Locate every leukocyte (white blood cell).
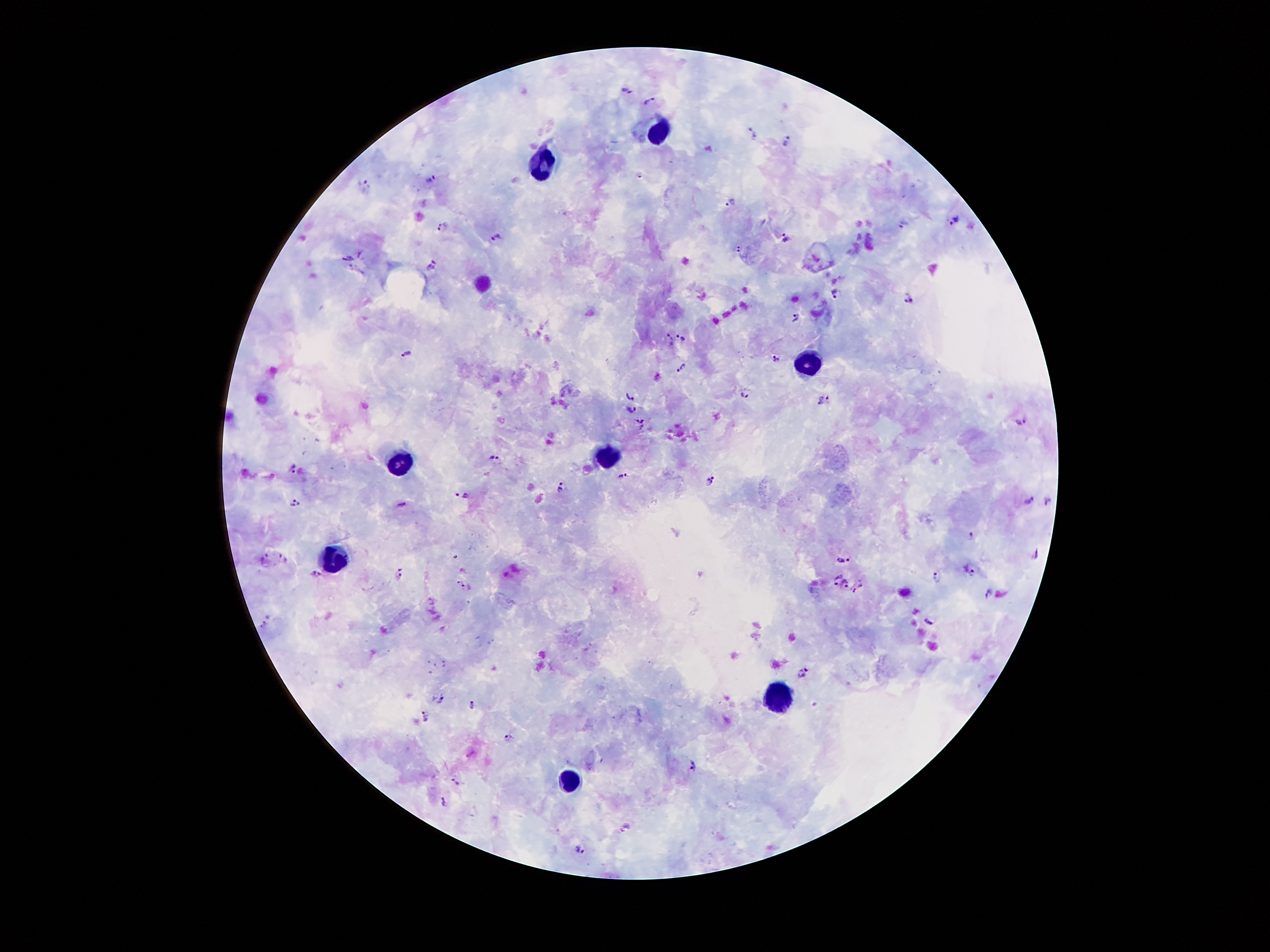

Approximate centers as (x, y) in pixels.
Leukocytes: (661, 129), (542, 161), (805, 367), (604, 456), (399, 459), (339, 554), (780, 700), (569, 781).

Malaria parasite locations: (626, 91), (650, 102), (753, 135), (787, 140), (640, 175), (431, 178), (365, 182), (731, 200), (955, 220), (904, 223), (443, 228), (786, 235), (495, 236), (736, 247), (348, 258), (431, 268), (835, 291), (908, 298), (796, 317), (682, 337), (667, 340), (408, 353), (776, 358), (683, 366), (744, 394), (629, 396), (825, 403), (632, 410), (1020, 419), (643, 423), (495, 457), (292, 467), (623, 476), (711, 479), (560, 487), (462, 494), (1028, 499), (1049, 500), (403, 503), (296, 504), (972, 534), (1036, 555), (284, 556), (263, 558), (845, 558), (971, 569), (318, 574), (400, 575), (935, 578), (838, 580), (844, 582), (461, 583), (858, 588), (988, 592), (928, 622), (264, 623), (803, 673), (439, 698), (472, 705), (425, 716), (508, 736), (692, 766), (456, 781), (442, 802), (625, 824), (579, 850). 100x magnification. Photographed through the microscope eyepiece with a smartphone camera. Image is 1270×952 pixels. Giemsa-stained preparation. Thick peripheral-blood smear. Single field of view. Patient malaria status: infected with Plasmodium falciparum.